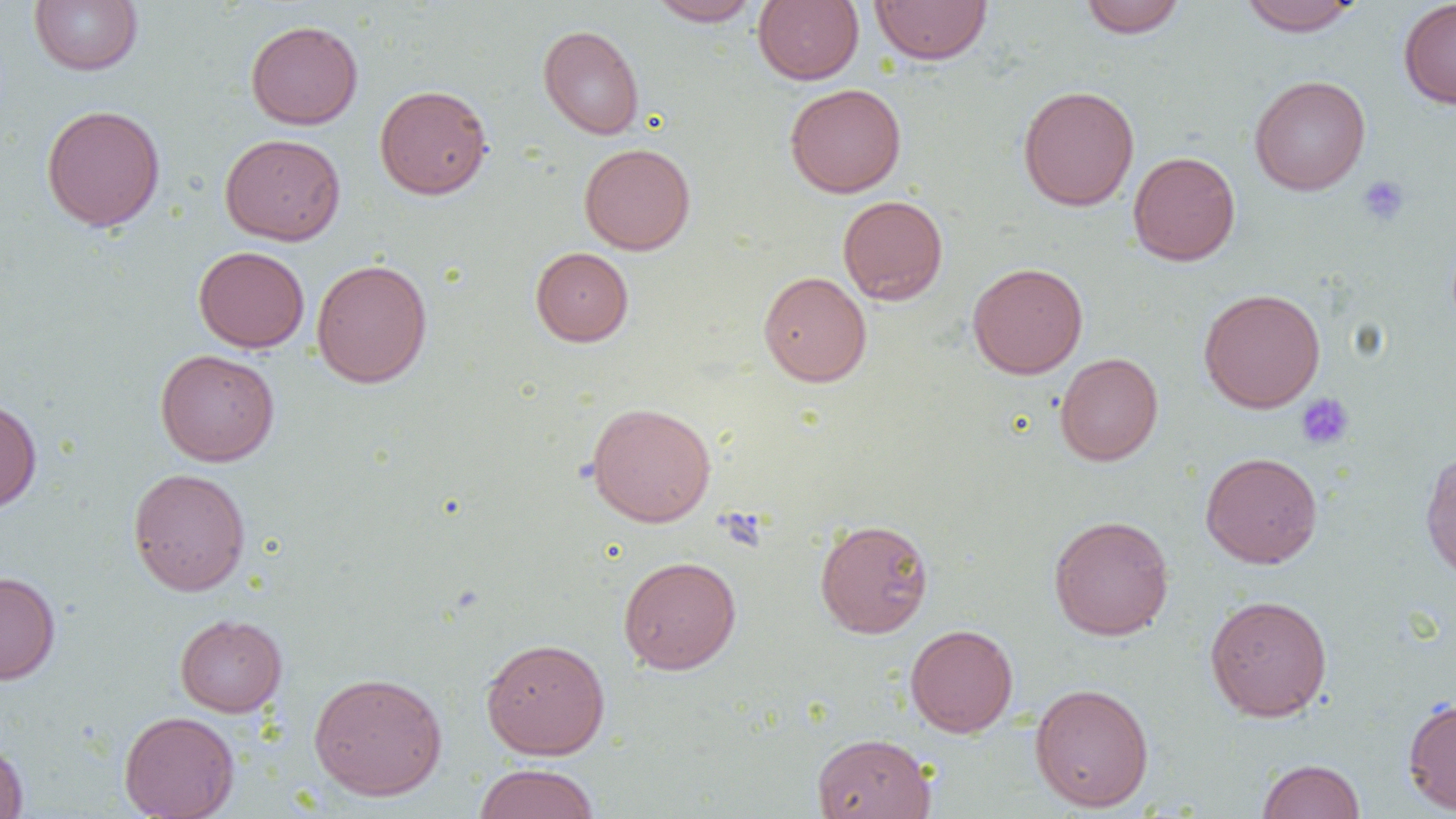

Summary:
  - Coordinate format: approximate bounding boxes as (x1, y1, x2, y2) in pixels
  - Platelet locations: (1357, 175, 1410, 227), (1296, 393, 1354, 450)
  - Uninfected red blood cell locations: (753, 0, 864, 85), (1079, 0, 1186, 38), (1238, 0, 1363, 36), (1398, 0, 1456, 109), (29, 1, 143, 75), (648, 1, 763, 26), (869, 1, 993, 65), (245, 19, 363, 130), (538, 24, 645, 139), (1249, 75, 1371, 195), (784, 83, 907, 198), (375, 84, 492, 199), (1018, 85, 1140, 212), (40, 104, 166, 232), (220, 133, 345, 245), (579, 142, 695, 254), (1128, 150, 1241, 266), (837, 194, 948, 305), (193, 246, 310, 352), (531, 246, 633, 346), (311, 258, 432, 388), (967, 261, 1088, 379), (758, 270, 872, 387), (1198, 288, 1326, 413), (156, 349, 279, 466), (1055, 352, 1164, 466), (0, 397, 42, 514), (586, 401, 717, 527), (1420, 448, 1456, 582), (1200, 452, 1323, 568), (128, 467, 251, 596), (1048, 514, 1174, 640), (814, 518, 934, 638), (618, 555, 742, 674), (0, 571, 60, 684), (1204, 594, 1333, 722), (174, 613, 288, 717), (905, 623, 1019, 737), (481, 637, 610, 759), (308, 671, 448, 800), (1030, 682, 1154, 812), (1403, 696, 1456, 815), (119, 710, 240, 819), (812, 732, 936, 819), (0, 738, 29, 819), (1257, 758, 1365, 818), (472, 763, 600, 819)
  - Slide-level diagnosis: negative for blood parasites
  - Image size: 1456×819 pixels
  - Magnification: 1000x
  - Modality: light microscopy
  - Preparation: thin blood smear
  - Field of view: one of a larger specimen